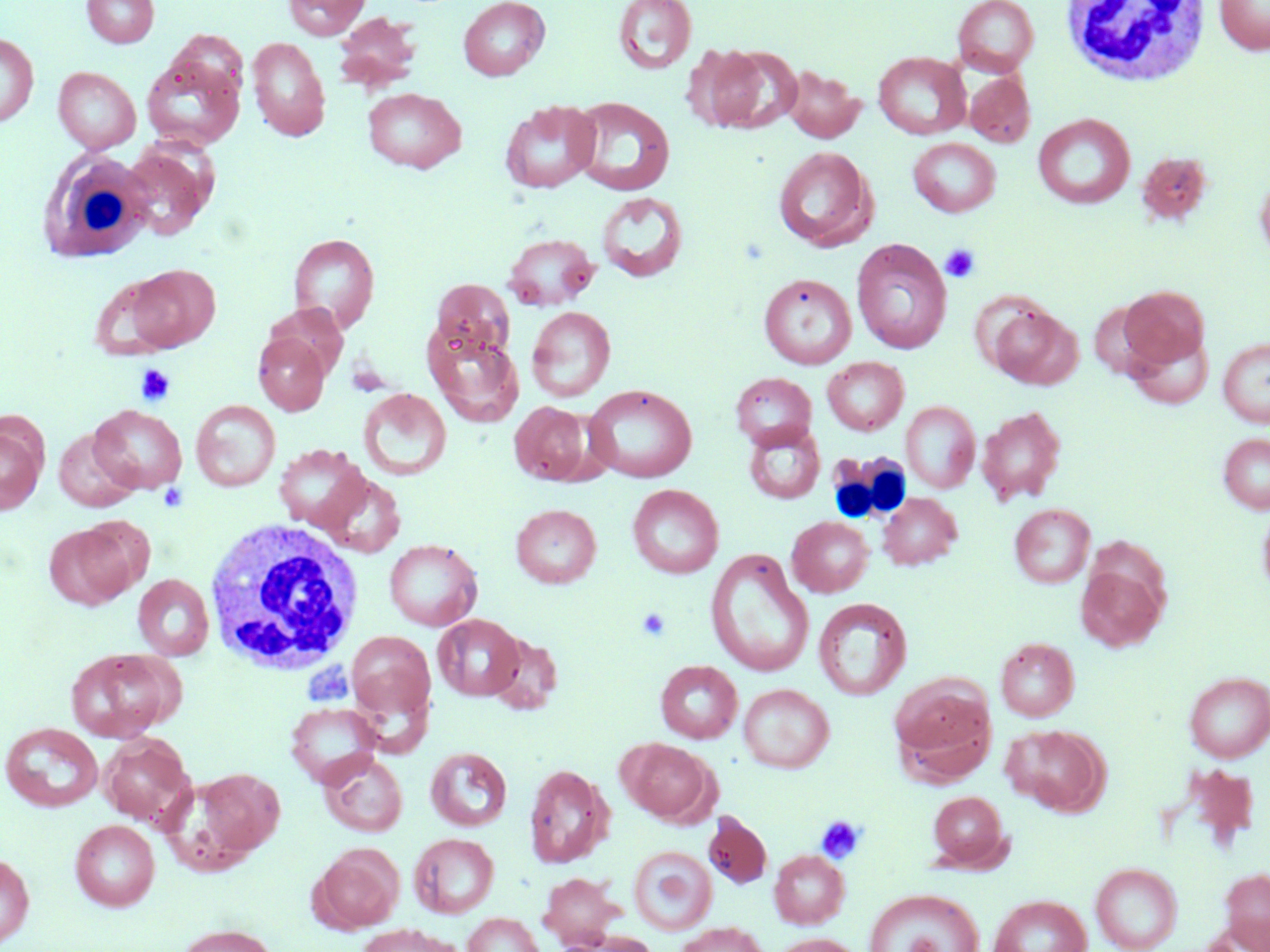
{
  "slide_level_diagnosis": "negative for blood parasites",
  "image_size": "1270×952 pixels",
  "white_blood_cell_locations": "approximate bounding boxes as (x1, y1, x2, y2) in pixels: (1060, 2, 1211, 88), (37, 144, 154, 261), (825, 450, 911, 525), (202, 518, 366, 675)",
  "platelet_locations": "approximate bounding boxes as (x1, y1, x2, y2) in pixels: (940, 243, 980, 282), (136, 364, 176, 406), (636, 607, 671, 641), (299, 657, 354, 708), (816, 816, 865, 864)",
  "modality": "optical microscopy",
  "uninfected_red_blood_cell_locations": "approximate bounding boxes as (x1, y1, x2, y2) in pixels: (82, 0, 159, 48), (283, 0, 370, 39), (458, 0, 550, 81), (612, 0, 697, 75), (952, 0, 1039, 76), (1214, 0, 1270, 55), (333, 12, 422, 92), (0, 33, 38, 128), (247, 36, 331, 142), (712, 44, 803, 133), (874, 51, 970, 139), (141, 53, 246, 151), (780, 65, 865, 143), (53, 67, 141, 153), (965, 71, 1035, 147), (361, 87, 467, 173), (570, 96, 675, 195), (500, 100, 602, 194), (1033, 113, 1135, 209), (908, 137, 1001, 217), (121, 142, 218, 241), (773, 146, 876, 251), (1138, 153, 1215, 225), (1255, 167, 1270, 266), (596, 191, 688, 282), (288, 233, 380, 333), (503, 233, 598, 310), (851, 239, 952, 354), (122, 264, 221, 353), (758, 273, 857, 369), (431, 279, 514, 360), (1119, 285, 1210, 371), (987, 302, 1081, 389), (527, 306, 616, 402), (425, 328, 524, 427), (1125, 329, 1213, 409), (253, 332, 329, 415), (1218, 338, 1270, 427), (822, 357, 909, 435), (731, 372, 816, 448), (584, 384, 697, 483), (358, 388, 452, 480), (191, 400, 281, 491), (902, 401, 980, 493), (509, 402, 592, 485), (89, 404, 187, 494), (977, 406, 1066, 505), (0, 421, 45, 515), (742, 422, 826, 504), (53, 427, 140, 512), (1218, 432, 1270, 513), (273, 444, 370, 532), (318, 471, 406, 558), (628, 484, 724, 578), (878, 492, 962, 570), (1257, 498, 1270, 600), (1009, 503, 1094, 588), (511, 504, 601, 588), (787, 516, 873, 597), (45, 523, 136, 610), (383, 539, 483, 631), (706, 549, 814, 678), (1075, 562, 1168, 652), (133, 574, 214, 660), (814, 597, 912, 701), (433, 614, 525, 701), (346, 630, 435, 721), (487, 632, 563, 714), (995, 637, 1079, 721), (66, 648, 179, 742), (655, 660, 742, 743), (1184, 671, 1270, 763), (890, 678, 997, 783), (739, 684, 834, 773), (285, 701, 382, 787), (1, 722, 103, 812), (1003, 724, 1108, 816), (99, 734, 195, 828), (621, 739, 716, 825), (425, 747, 512, 831), (319, 751, 408, 837), (523, 764, 613, 868), (1183, 764, 1259, 847), (195, 768, 285, 857), (928, 791, 1008, 869), (704, 812, 771, 888), (70, 819, 160, 911), (409, 833, 499, 918), (312, 843, 404, 932), (628, 846, 717, 935), (769, 850, 849, 928), (0, 853, 34, 947), (1091, 862, 1182, 952), (1219, 867, 1270, 950), (538, 871, 624, 948), (864, 888, 984, 952), (989, 895, 1091, 952), (463, 912, 544, 952), (675, 922, 769, 952), (173, 923, 279, 952), (357, 924, 454, 952), (556, 930, 659, 952), (771, 933, 864, 952)",
  "stain": "May-Grünwald-Giemsa",
  "preparation": "thin blood smear",
  "field_of_view": "single",
  "magnification": "1000x"
}